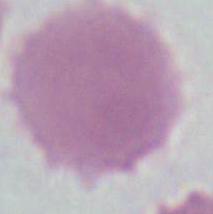 Micrograph. A red blood cell is shown. Captured at 1000x magnification.